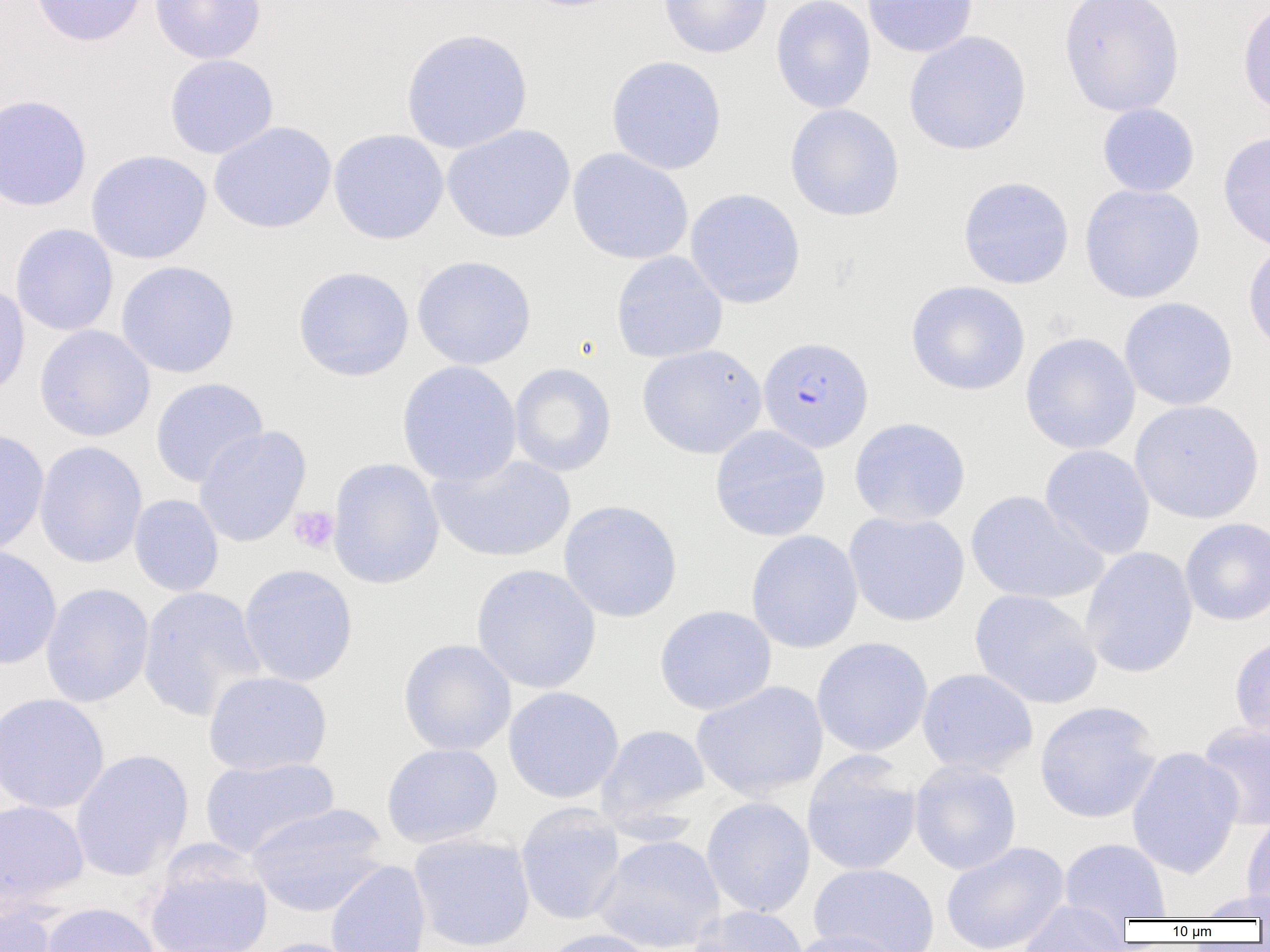

Summary:
  - Coordinate format: approximate bounding boxes as named x1/y1/x2/y2 corners in pixels
  - Platelet locations: (x1=288, y1=506, x2=339, y2=554)
  - Uninfected red blood cell locations: (x1=30, y1=0, x2=148, y2=47), (x1=149, y1=0, x2=266, y2=64), (x1=513, y1=0, x2=636, y2=13), (x1=658, y1=0, x2=773, y2=59), (x1=771, y1=0, x2=876, y2=114), (x1=862, y1=0, x2=978, y2=58), (x1=1059, y1=0, x2=1185, y2=117), (x1=1237, y1=0, x2=1270, y2=119), (x1=400, y1=28, x2=533, y2=154), (x1=904, y1=30, x2=1031, y2=155), (x1=164, y1=54, x2=279, y2=159), (x1=605, y1=55, x2=727, y2=175), (x1=0, y1=94, x2=92, y2=212), (x1=1097, y1=103, x2=1200, y2=198), (x1=784, y1=104, x2=905, y2=221), (x1=209, y1=121, x2=337, y2=234), (x1=442, y1=124, x2=575, y2=243), (x1=328, y1=128, x2=449, y2=244), (x1=1218, y1=131, x2=1270, y2=254), (x1=567, y1=148, x2=694, y2=265), (x1=86, y1=150, x2=212, y2=264), (x1=958, y1=176, x2=1074, y2=289), (x1=1079, y1=184, x2=1205, y2=304), (x1=684, y1=188, x2=806, y2=308), (x1=10, y1=223, x2=119, y2=336), (x1=1243, y1=240, x2=1270, y2=358), (x1=611, y1=251, x2=728, y2=363), (x1=411, y1=255, x2=537, y2=370), (x1=116, y1=261, x2=240, y2=378), (x1=292, y1=266, x2=415, y2=381), (x1=906, y1=279, x2=1030, y2=396), (x1=0, y1=280, x2=31, y2=401), (x1=1118, y1=297, x2=1238, y2=411), (x1=34, y1=325, x2=155, y2=442), (x1=1020, y1=332, x2=1141, y2=454), (x1=637, y1=344, x2=767, y2=459), (x1=396, y1=360, x2=522, y2=487), (x1=509, y1=363, x2=616, y2=476), (x1=150, y1=377, x2=269, y2=488), (x1=1130, y1=400, x2=1265, y2=523), (x1=848, y1=417, x2=971, y2=527), (x1=194, y1=425, x2=311, y2=548), (x1=709, y1=425, x2=831, y2=541), (x1=0, y1=428, x2=50, y2=556), (x1=34, y1=441, x2=148, y2=569), (x1=1040, y1=444, x2=1155, y2=560), (x1=428, y1=453, x2=575, y2=563), (x1=327, y1=457, x2=445, y2=589), (x1=966, y1=490, x2=1106, y2=605), (x1=129, y1=494, x2=224, y2=597), (x1=558, y1=499, x2=682, y2=622), (x1=844, y1=511, x2=970, y2=627), (x1=1180, y1=517, x2=1270, y2=625), (x1=745, y1=529, x2=864, y2=653), (x1=0, y1=544, x2=62, y2=670), (x1=1080, y1=547, x2=1199, y2=678), (x1=238, y1=563, x2=359, y2=687), (x1=471, y1=563, x2=601, y2=694), (x1=39, y1=582, x2=154, y2=708), (x1=137, y1=586, x2=266, y2=721), (x1=969, y1=589, x2=1103, y2=709), (x1=654, y1=605, x2=777, y2=715), (x1=1230, y1=633, x2=1270, y2=747), (x1=811, y1=637, x2=933, y2=756), (x1=398, y1=639, x2=516, y2=756), (x1=916, y1=668, x2=1038, y2=776), (x1=203, y1=671, x2=332, y2=776), (x1=691, y1=680, x2=828, y2=800), (x1=503, y1=686, x2=624, y2=803), (x1=0, y1=693, x2=110, y2=815), (x1=1034, y1=700, x2=1163, y2=823), (x1=1197, y1=721, x2=1270, y2=831), (x1=597, y1=724, x2=711, y2=826), (x1=381, y1=742, x2=502, y2=847), (x1=1127, y1=746, x2=1244, y2=879), (x1=70, y1=749, x2=194, y2=882), (x1=802, y1=753, x2=922, y2=876), (x1=199, y1=756, x2=340, y2=859), (x1=909, y1=759, x2=1022, y2=875), (x1=701, y1=797, x2=816, y2=918), (x1=0, y1=800, x2=89, y2=909), (x1=246, y1=803, x2=390, y2=917), (x1=516, y1=803, x2=626, y2=925), (x1=1241, y1=810, x2=1270, y2=917), (x1=408, y1=833, x2=535, y2=952), (x1=593, y1=834, x2=725, y2=951), (x1=1059, y1=838, x2=1172, y2=920), (x1=940, y1=841, x2=1070, y2=952), (x1=145, y1=851, x2=273, y2=952), (x1=325, y1=859, x2=432, y2=952), (x1=808, y1=863, x2=940, y2=952), (x1=1191, y1=889, x2=1270, y2=921), (x1=1017, y1=902, x2=1132, y2=951), (x1=0, y1=903, x2=61, y2=952), (x1=39, y1=903, x2=161, y2=952), (x1=690, y1=905, x2=808, y2=952), (x1=539, y1=928, x2=661, y2=952), (x1=786, y1=929, x2=909, y2=952), (x1=250, y1=937, x2=369, y2=952)
  - Plasmodium falciparum-infected red blood cell locations: (x1=758, y1=336, x2=873, y2=452)
  - Slide-level diagnosis: Plasmodium falciparum
  - Image size: 1270×952 pixels
  - Preparation: thin blood smear
  - Field of view: single
  - Modality: light microscopy
  - Magnification: 1000x